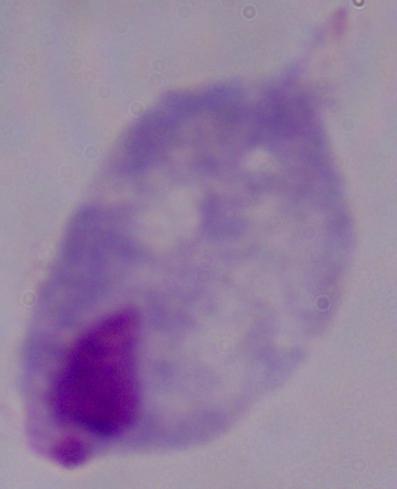

Photomicrograph. A trichomonad is seen. 1000x magnification.